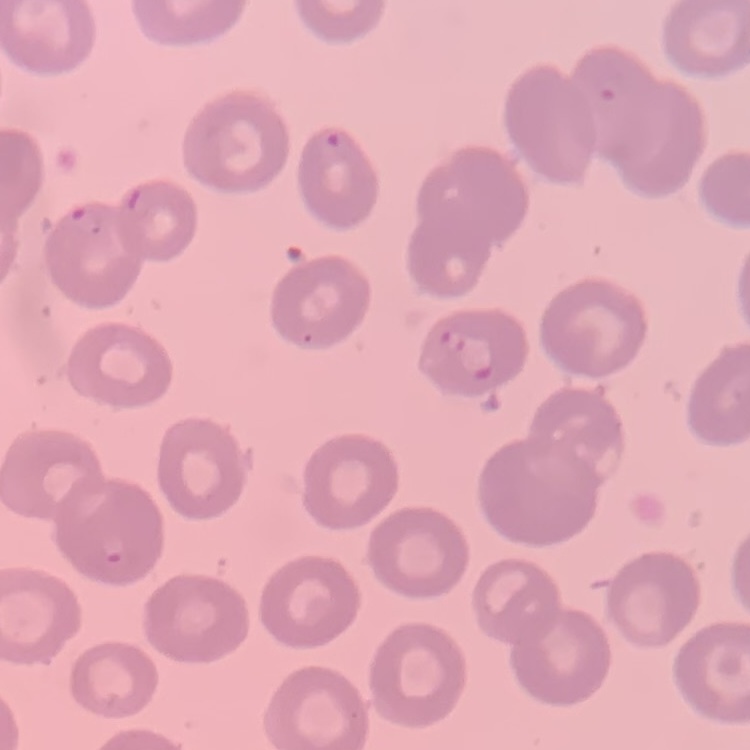
Summary:
  - Erythrocyte morphology: no rouleaux formation
  - Image type: one tile cut from a larger photomicrograph
  - Preparation: thin blood smear
  - Stain: Field's or Giemsa